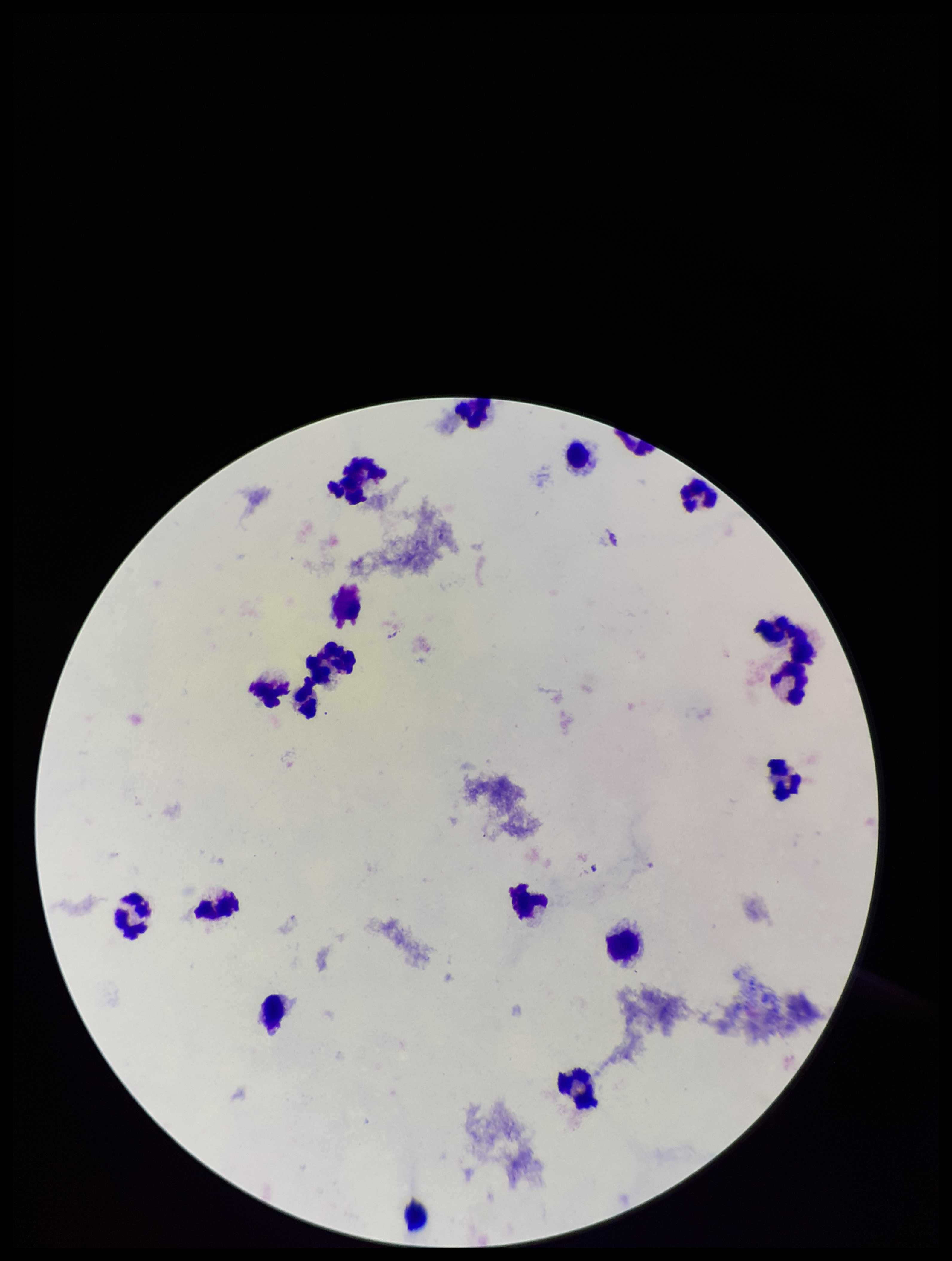
Summary:
  - Parasite count: 0
  - Leukocyte count: 19
  - Plasmodium parasites: none identified
  - Patient malaria status: negative
  - Stain: Giemsa
  - Image size: 952×1261 pixels
  - Preparation: thick smear
  - Field of view: one from this slide
  - Capture: smartphone photograph through the microscope eyepiece